Find the red blood cells and label each as P. falciparum-infected, uninfected, or of indeterminate infection status.
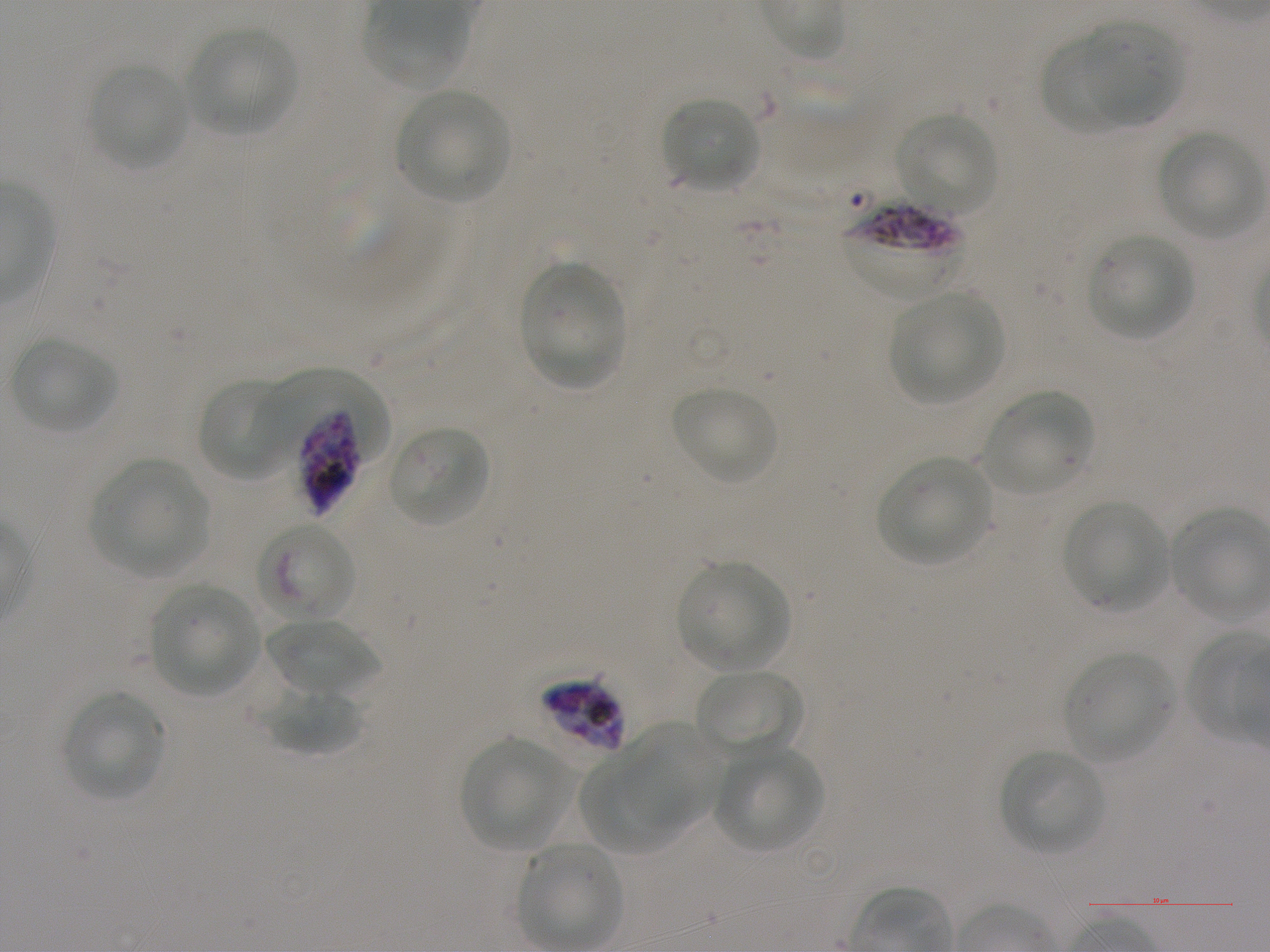
Approximate bounding rectangles given as corner coordinates in pixels from the top-left. Not every red blood cell is marked.
Infected red blood cells: (x1=842, y1=202, x2=968, y2=300), (x1=297, y1=398, x2=362, y2=516).
Red blood cells of indeterminate infection status: (x1=260, y1=367, x2=384, y2=505), (x1=259, y1=520, x2=357, y2=621), (x1=541, y1=678, x2=626, y2=753).
Uninfected red blood cells: (x1=1078, y1=21, x2=1183, y2=125), (x1=185, y1=26, x2=299, y2=136), (x1=1040, y1=34, x2=1139, y2=134), (x1=89, y1=63, x2=190, y2=170), (x1=395, y1=88, x2=509, y2=201), (x1=661, y1=96, x2=762, y2=192), (x1=897, y1=112, x2=999, y2=215), (x1=1158, y1=131, x2=1264, y2=238), (x1=1089, y1=233, x2=1193, y2=339), (x1=519, y1=261, x2=625, y2=389), (x1=889, y1=292, x2=1004, y2=404), (x1=10, y1=337, x2=118, y2=434), (x1=197, y1=378, x2=291, y2=480), (x1=672, y1=385, x2=778, y2=484), (x1=982, y1=390, x2=1097, y2=495), (x1=388, y1=424, x2=490, y2=527), (x1=877, y1=455, x2=994, y2=565), (x1=90, y1=457, x2=211, y2=578), (x1=1062, y1=499, x2=1170, y2=612), (x1=677, y1=560, x2=790, y2=671), (x1=149, y1=583, x2=259, y2=695), (x1=266, y1=617, x2=379, y2=697), (x1=1064, y1=651, x2=1173, y2=763), (x1=694, y1=668, x2=803, y2=757), (x1=265, y1=686, x2=363, y2=757), (x1=61, y1=691, x2=166, y2=801), (x1=624, y1=722, x2=727, y2=833), (x1=459, y1=737, x2=572, y2=849), (x1=714, y1=745, x2=824, y2=852), (x1=1000, y1=749, x2=1105, y2=854), (x1=579, y1=750, x2=681, y2=856), (x1=518, y1=843, x2=622, y2=948).

Summary:
  - Field of view: one from this slide
  - Image size: 1270×952 pixels
  - Preparation: thin blood film
  - Donor blood group: A+
  - Stain: Giemsa
  - Culture: in-vitro P. falciparum strain NF54, static
  - Objective: 100x, oil immersion, numerical aperture 1.25